Classify this cell by malaria status.
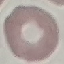
Uninfected.

capture: smartphone camera at the microscope eyepiece
image_type: cell patch, automatically extracted from a larger field of view and resized to 64 × 64 pixels
preparation: thin blood film
stain: Giemsa